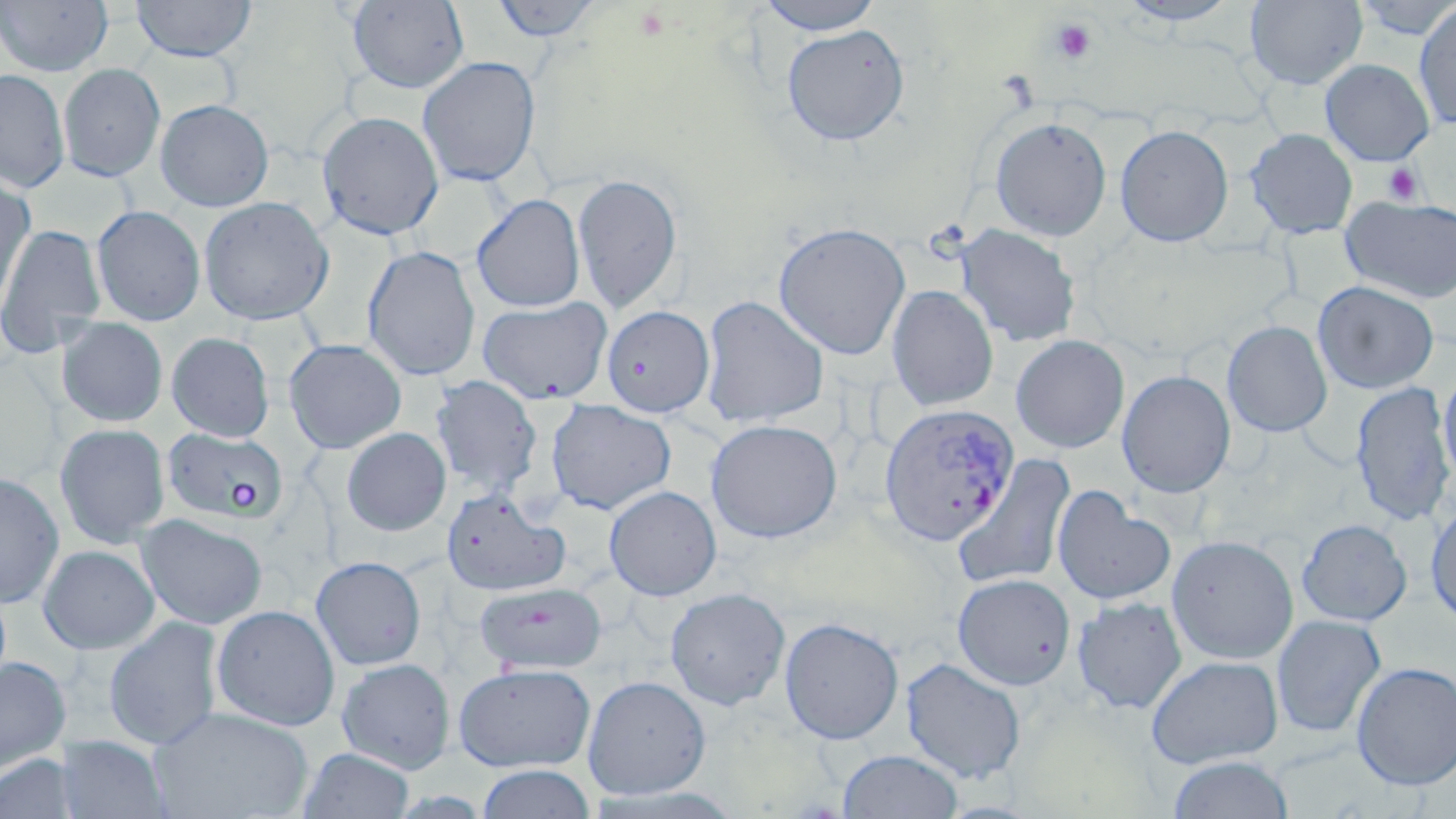
slide-level diagnosis = Plasmodium vivax
stain = May-Grünwald-Giemsa
platelet locations = approximate bounding boxes as named x1/y1/x2/y2 corners in pixels: (x1=1049, y1=18, x2=1097, y2=64), (x1=1383, y1=163, x2=1422, y2=205)
uninfected red blood cell locations = approximate bounding boxes as named x1/y1/x2/y2 corners in pixels: (x1=1, y1=0, x2=112, y2=77), (x1=131, y1=0, x2=257, y2=62), (x1=754, y1=0, x2=885, y2=36), (x1=1114, y1=0, x2=1245, y2=26), (x1=1245, y1=0, x2=1368, y2=89), (x1=1352, y1=0, x2=1456, y2=41), (x1=346, y1=1, x2=470, y2=93), (x1=487, y1=1, x2=606, y2=42), (x1=1414, y1=2, x2=1456, y2=130), (x1=781, y1=23, x2=910, y2=146), (x1=417, y1=56, x2=541, y2=187), (x1=1320, y1=58, x2=1435, y2=166), (x1=58, y1=63, x2=166, y2=182), (x1=0, y1=68, x2=70, y2=193), (x1=155, y1=99, x2=274, y2=211), (x1=317, y1=111, x2=444, y2=240), (x1=989, y1=116, x2=1112, y2=240), (x1=1115, y1=124, x2=1234, y2=246), (x1=1244, y1=127, x2=1358, y2=239), (x1=573, y1=173, x2=684, y2=313), (x1=0, y1=175, x2=36, y2=316), (x1=471, y1=193, x2=585, y2=313), (x1=199, y1=196, x2=334, y2=326), (x1=1341, y1=196, x2=1456, y2=304), (x1=92, y1=205, x2=205, y2=326), (x1=773, y1=222, x2=911, y2=360), (x1=0, y1=224, x2=106, y2=358), (x1=953, y1=224, x2=1081, y2=347), (x1=362, y1=245, x2=481, y2=382), (x1=1313, y1=281, x2=1439, y2=394), (x1=887, y1=285, x2=998, y2=411), (x1=700, y1=295, x2=829, y2=428), (x1=478, y1=297, x2=611, y2=404), (x1=602, y1=305, x2=715, y2=417), (x1=56, y1=316, x2=168, y2=428), (x1=1222, y1=320, x2=1332, y2=437), (x1=166, y1=332, x2=274, y2=442), (x1=1010, y1=334, x2=1130, y2=453), (x1=284, y1=338, x2=406, y2=453), (x1=1438, y1=369, x2=1456, y2=491), (x1=1117, y1=370, x2=1235, y2=497), (x1=429, y1=375, x2=544, y2=499), (x1=1351, y1=380, x2=1454, y2=526), (x1=546, y1=399, x2=676, y2=515), (x1=706, y1=419, x2=842, y2=543), (x1=54, y1=423, x2=170, y2=549), (x1=161, y1=426, x2=287, y2=525), (x1=342, y1=427, x2=451, y2=536), (x1=952, y1=454, x2=1076, y2=592), (x1=0, y1=472, x2=64, y2=609), (x1=604, y1=485, x2=722, y2=601), (x1=441, y1=487, x2=571, y2=596), (x1=1052, y1=488, x2=1176, y2=606), (x1=1426, y1=502, x2=1456, y2=627), (x1=138, y1=514, x2=267, y2=629), (x1=1297, y1=518, x2=1412, y2=626), (x1=1167, y1=534, x2=1298, y2=665), (x1=38, y1=545, x2=160, y2=654), (x1=310, y1=556, x2=426, y2=670), (x1=952, y1=573, x2=1076, y2=690), (x1=474, y1=581, x2=606, y2=674), (x1=665, y1=588, x2=790, y2=710), (x1=1072, y1=596, x2=1187, y2=715), (x1=211, y1=604, x2=340, y2=731), (x1=1272, y1=615, x2=1386, y2=739), (x1=104, y1=617, x2=223, y2=750), (x1=780, y1=618, x2=904, y2=744), (x1=1146, y1=655, x2=1283, y2=769), (x1=0, y1=657, x2=70, y2=773), (x1=336, y1=658, x2=455, y2=774), (x1=901, y1=658, x2=1025, y2=784), (x1=1351, y1=661, x2=1456, y2=791), (x1=453, y1=663, x2=595, y2=772), (x1=583, y1=675, x2=711, y2=798), (x1=147, y1=706, x2=313, y2=819), (x1=59, y1=735, x2=168, y2=819), (x1=299, y1=747, x2=415, y2=819), (x1=837, y1=749, x2=964, y2=819), (x1=0, y1=754, x2=66, y2=819), (x1=1167, y1=754, x2=1294, y2=819), (x1=477, y1=764, x2=597, y2=819)
preparation = thin blood smear
Plasmodium vivax-infected red blood cell locations = approximate bounding boxes as named x1/y1/x2/y2 corners in pixels: (x1=878, y1=403, x2=1019, y2=547)
field of view = one of a larger specimen
magnification = 1000x
modality = light microscopy
image size = 1456×819 pixels